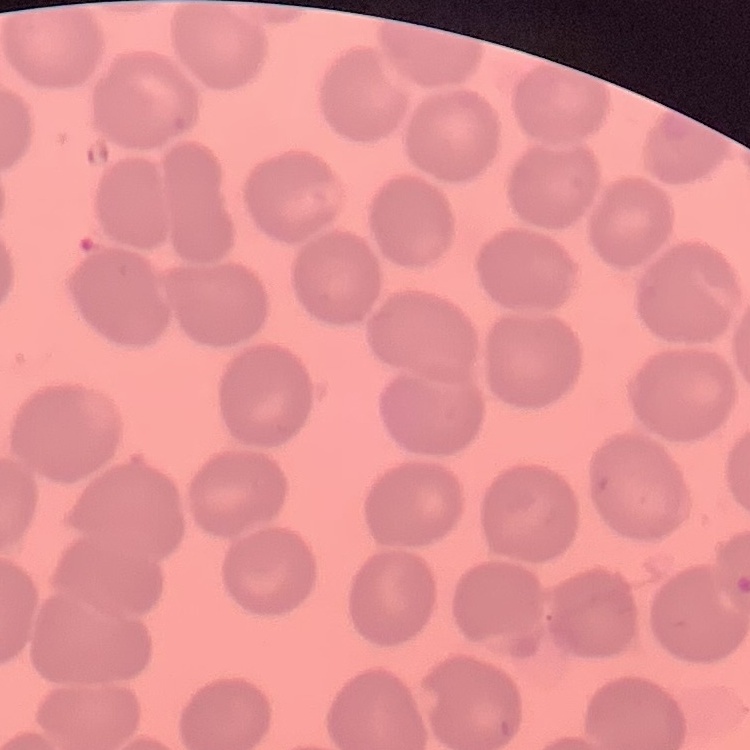

Summary:
  - Erythrocyte morphology: no rouleaux formation
  - Preparation: thin blood film
  - Stain: Field's or Giemsa
  - Image type: square crop of a larger photomicrograph